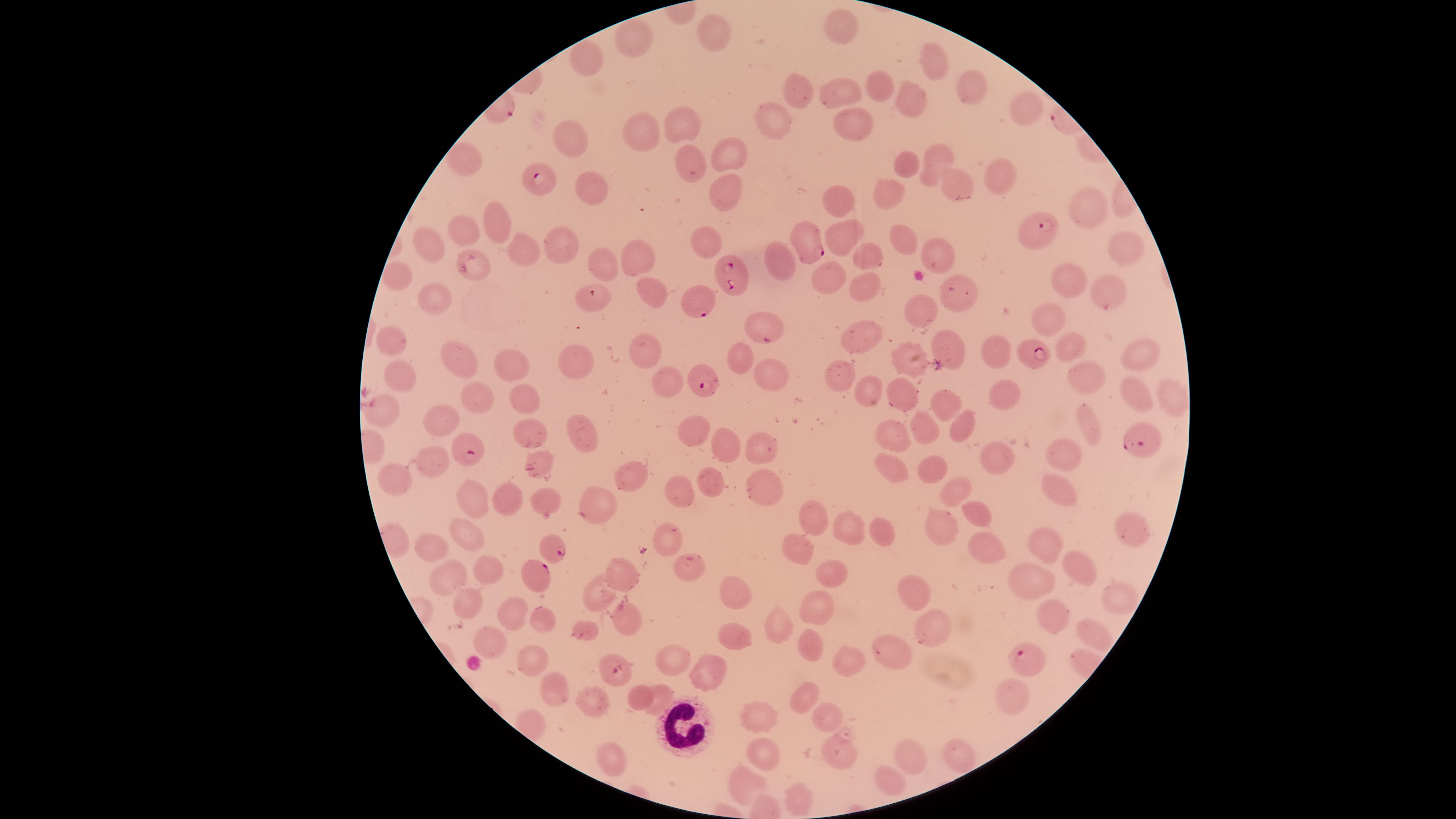
{
  "field_of_view": "single",
  "white_blood_cells": "approximate marker points as (x, y) in pixels: (689, 722)",
  "presence": "malaria parasites detected",
  "visible_region": "circular",
  "species": "Plasmodium falciparum",
  "capture": "smartphone photograph through the microscope eyepiece",
  "uninfected_red_blood_cells": "approximate marker points as (x, y) in pixels: (842, 26), (709, 28), (638, 39), (587, 57), (929, 61), (878, 82), (800, 91), (842, 92), (969, 92), (916, 101), (1024, 116), (684, 122), (771, 123), (854, 123), (644, 132), (571, 141), (724, 152), (933, 155), (466, 162), (694, 162), (905, 171), (1000, 173), (954, 186), (586, 187), (722, 187), (840, 197), (892, 197), (1084, 209), (495, 219), (842, 234), (466, 239), (905, 239), (564, 241), (707, 241), (526, 243), (1128, 248), (430, 251), (937, 251), (638, 253), (870, 255), (600, 262), (773, 263), (476, 267), (397, 278), (1069, 279), (826, 280), (865, 287), (655, 290), (965, 293), (1108, 293), (438, 300), (598, 301), (921, 309), (1045, 319), (859, 337), (388, 339), (1068, 341), (643, 344), (947, 346), (995, 351), (1137, 354), (462, 355), (741, 357), (904, 359), (569, 360), (505, 368), (772, 371), (666, 373), (401, 375), (843, 375), (1085, 376), (866, 388), (529, 394), (1005, 395), (1135, 395), (899, 397), (488, 398), (1169, 398), (940, 406), (383, 412), (442, 420), (1088, 423), (924, 429), (965, 430), (689, 431), (530, 436), (892, 436), (577, 440), (721, 446), (758, 446), (1065, 453), (996, 458), (425, 462), (890, 468), (934, 472), (539, 474), (629, 476), (395, 478), (708, 480), (762, 488), (1058, 488), (681, 491), (955, 491), (544, 496), (507, 498), (468, 500), (595, 506), (974, 514), (813, 517), (463, 527), (843, 529), (943, 529), (880, 534), (1128, 534), (664, 536), (437, 545), (981, 545), (1048, 548), (792, 551), (485, 568), (1072, 569), (617, 572), (832, 572), (453, 574), (685, 574), (1032, 582), (597, 594), (730, 594), (919, 594), (468, 595), (1115, 595), (823, 608), (517, 612), (543, 614), (621, 615), (1053, 618), (930, 623), (776, 624), (1093, 631), (585, 634), (484, 637), (738, 639), (809, 645), (674, 654), (900, 654), (844, 663), (531, 666), (707, 671), (559, 690), (801, 692), (662, 694), (638, 697), (1012, 697), (590, 703), (826, 715), (758, 717), (835, 748), (765, 753), (607, 754), (904, 755), (955, 757), (883, 783), (742, 784), (792, 800)",
  "preparation": "thin blood film",
  "parasitized_red_blood_cells": "approximate marker points as (x, y) in pixels: (539, 178), (1037, 232), (805, 246), (739, 272), (699, 301), (762, 326), (1030, 351), (704, 380), (1141, 441), (470, 448), (551, 548), (535, 574), (1029, 662)",
  "image_size": "1456×819 pixels",
  "stain": "Giemsa"
}